Give the position of every Plasmodium parasite.
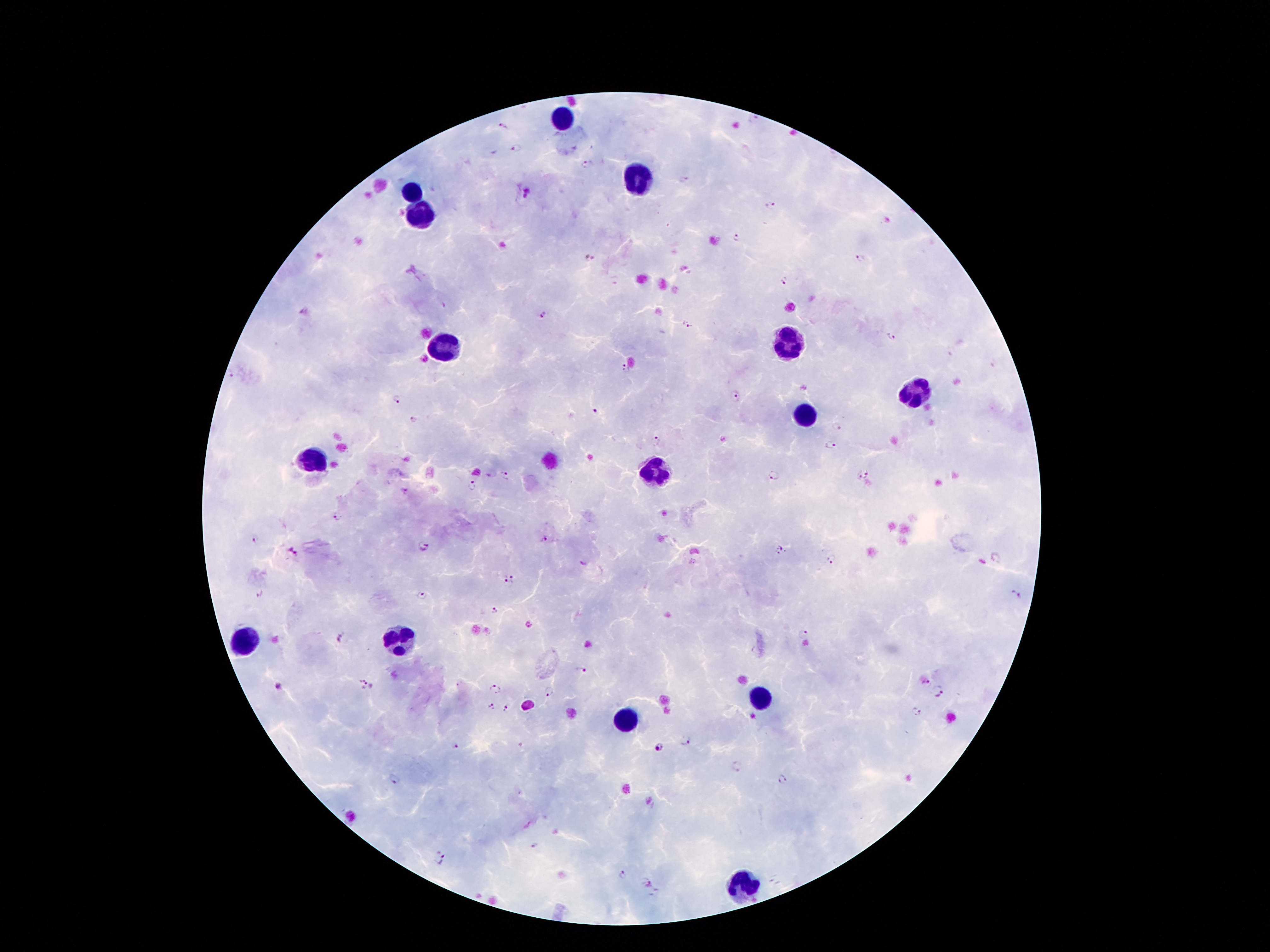
Approximate centers as (x, y) in pixels.
Plasmodium parasites: (756, 121), (503, 127), (519, 147), (587, 166), (683, 178), (771, 206), (737, 238), (588, 258), (861, 258), (783, 282), (542, 315), (686, 325), (891, 336), (624, 371), (231, 375), (736, 396), (397, 399), (595, 410), (413, 420), (838, 428), (657, 440), (829, 446), (869, 475), (506, 476), (773, 476), (859, 477), (472, 486), (336, 517), (259, 540), (541, 541), (424, 547), (779, 550), (292, 553), (995, 557), (833, 560), (583, 564), (511, 572), (508, 583), (260, 594), (421, 595), (1014, 595), (496, 612), (804, 633), (341, 639), (581, 671), (362, 678), (925, 681), (279, 686), (366, 688), (495, 688), (549, 691), (941, 693), (491, 706), (508, 707), (914, 712), (685, 740), (455, 744), (659, 748), (735, 767), (781, 778), (394, 779), (535, 845), (441, 860), (623, 874), (649, 883).

Summary:
  - Leukocyte locations: (565, 122), (635, 183), (413, 194), (425, 207), (791, 344), (445, 346), (915, 388), (805, 420), (315, 462), (655, 478), (243, 638), (401, 640), (759, 698), (625, 722), (743, 888)
  - Capture: smartphone camera through the microscope eyepiece
  - Patient malaria status: infected with Plasmodium falciparum
  - Preparation: thick blood film
  - Stain: Giemsa
  - Magnification: 100x
  - Image size: 1270×952 pixels
  - Field of view: single